Assess this cell for malaria.
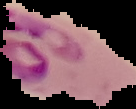
It is parasitized.

Summary:
  - Image size: 136×109 pixels
  - Preparation: thin blood smear
  - Image type: segmented cell region on a black background